Name the cell type shown.
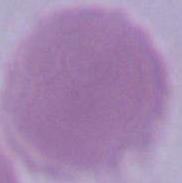

An erythrocyte.

Micrograph. Captured at 1000x magnification.